Identify the preparation type.
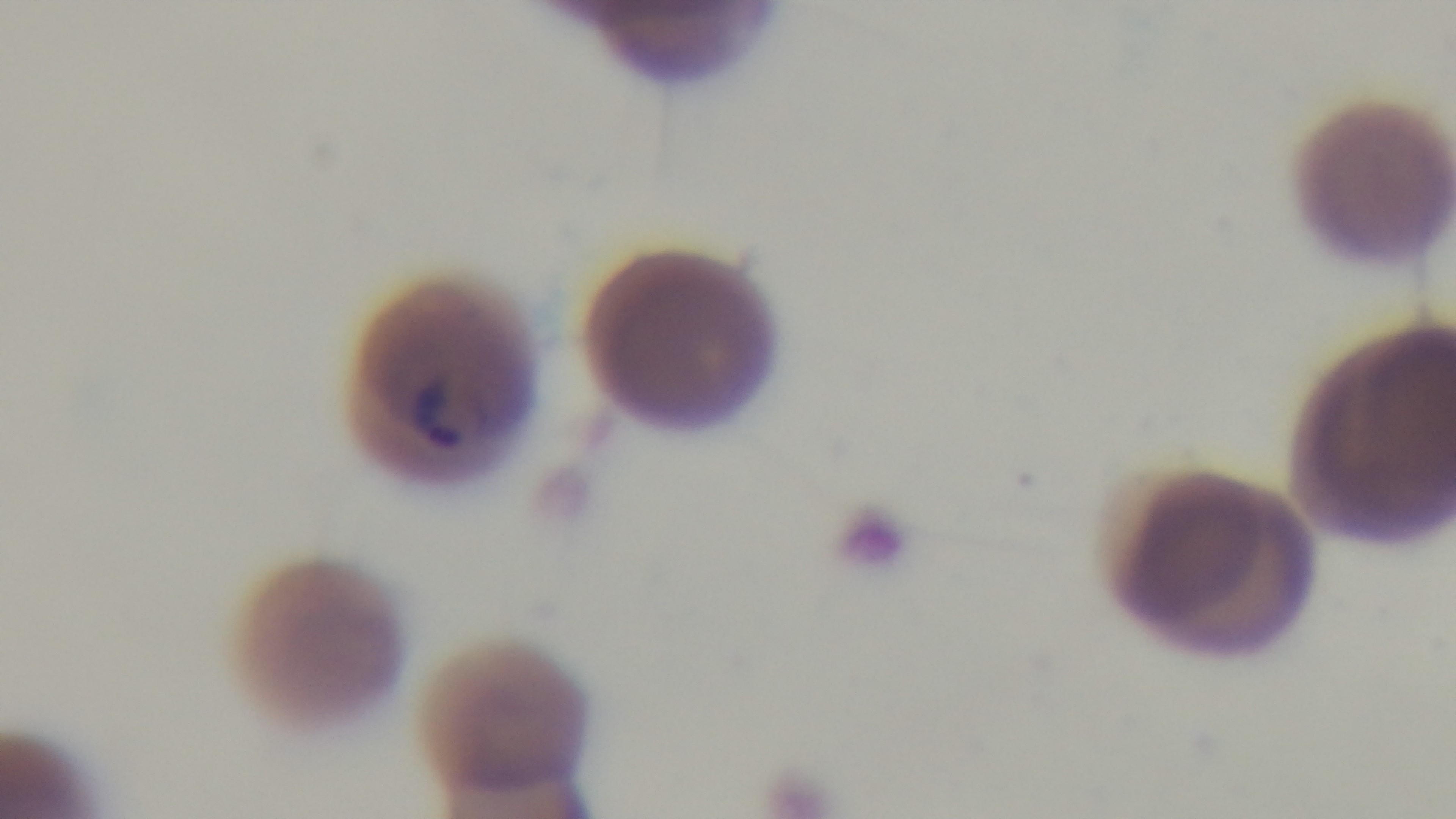

Thin.

stain = Giemsa
modality = light microscopy
capture = mounted 4K digital camera
field of view = one from the slide
malaria status = infected
objective = 100x oil immersion